Report the malaria status of this cell.
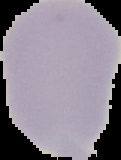

Uninfected.

{
  "preparation": "thin blood smear",
  "image_type": "cell region segmented out of the field of view; surrounding area masked to black",
  "image_size": "121×160 pixels"
}